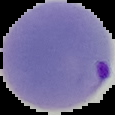

{
  "preparation": "thin blood smear",
  "image_type": "cell region segmented out of the field of view; surrounding area masked to black",
  "image_size": "115×115 pixels",
  "result": "Plasmodium parasites detected"
}